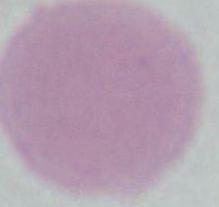

{
  "modality": "photomicrograph",
  "magnification": "1000x",
  "identification": "erythrocyte"
}